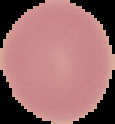 Result: negative for Plasmodium parasites. From a thin blood smear. Image is 115×124 pixels. Segmented cell region on a black background.